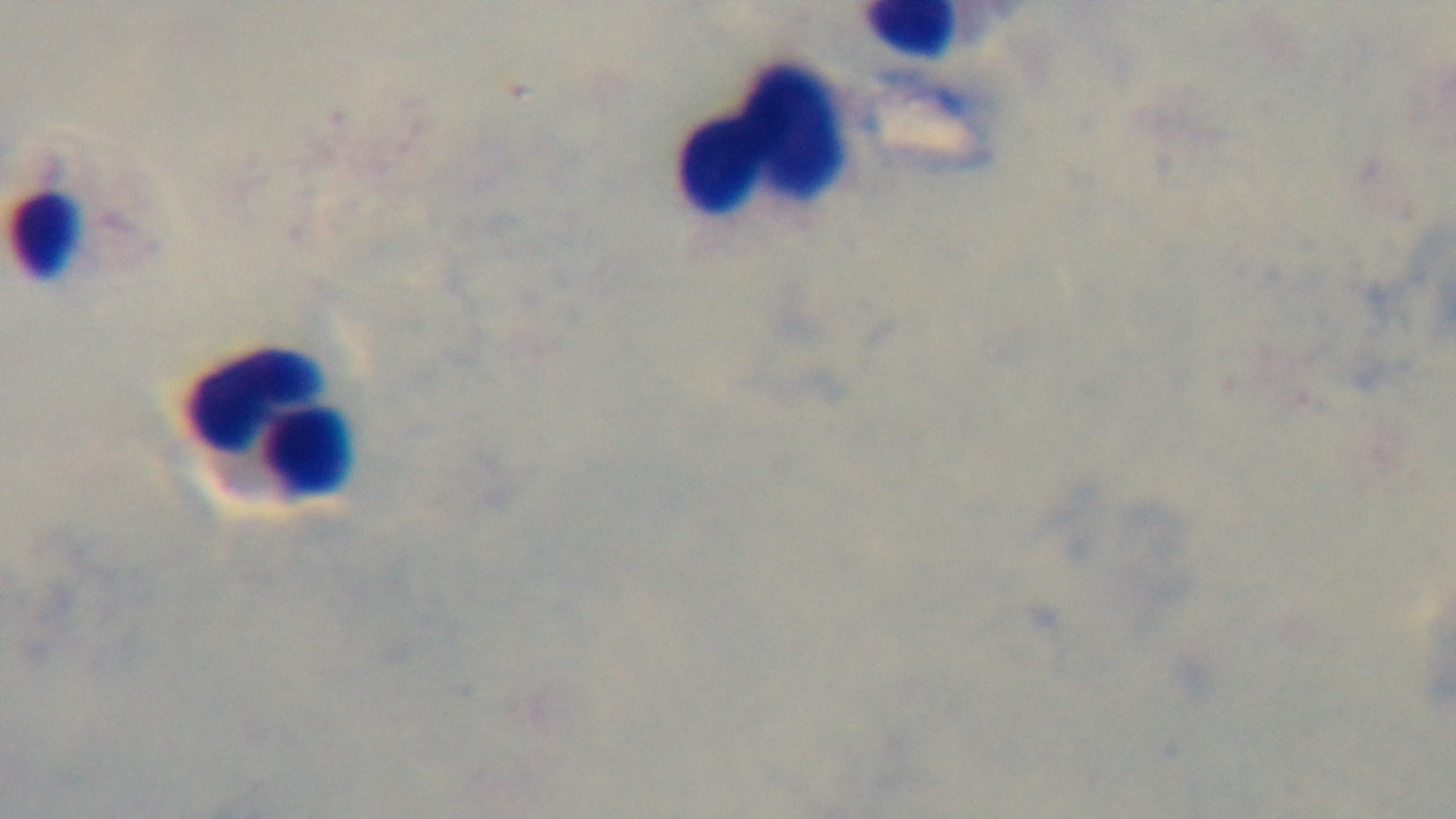
malaria status = negative
preparation = thick blood film
capture = mounted 4K digital camera
modality = light microscopy
stain = Giemsa
field of view = one from the slide
objective = 100x oil immersion